Locate and identify every blood parasite.
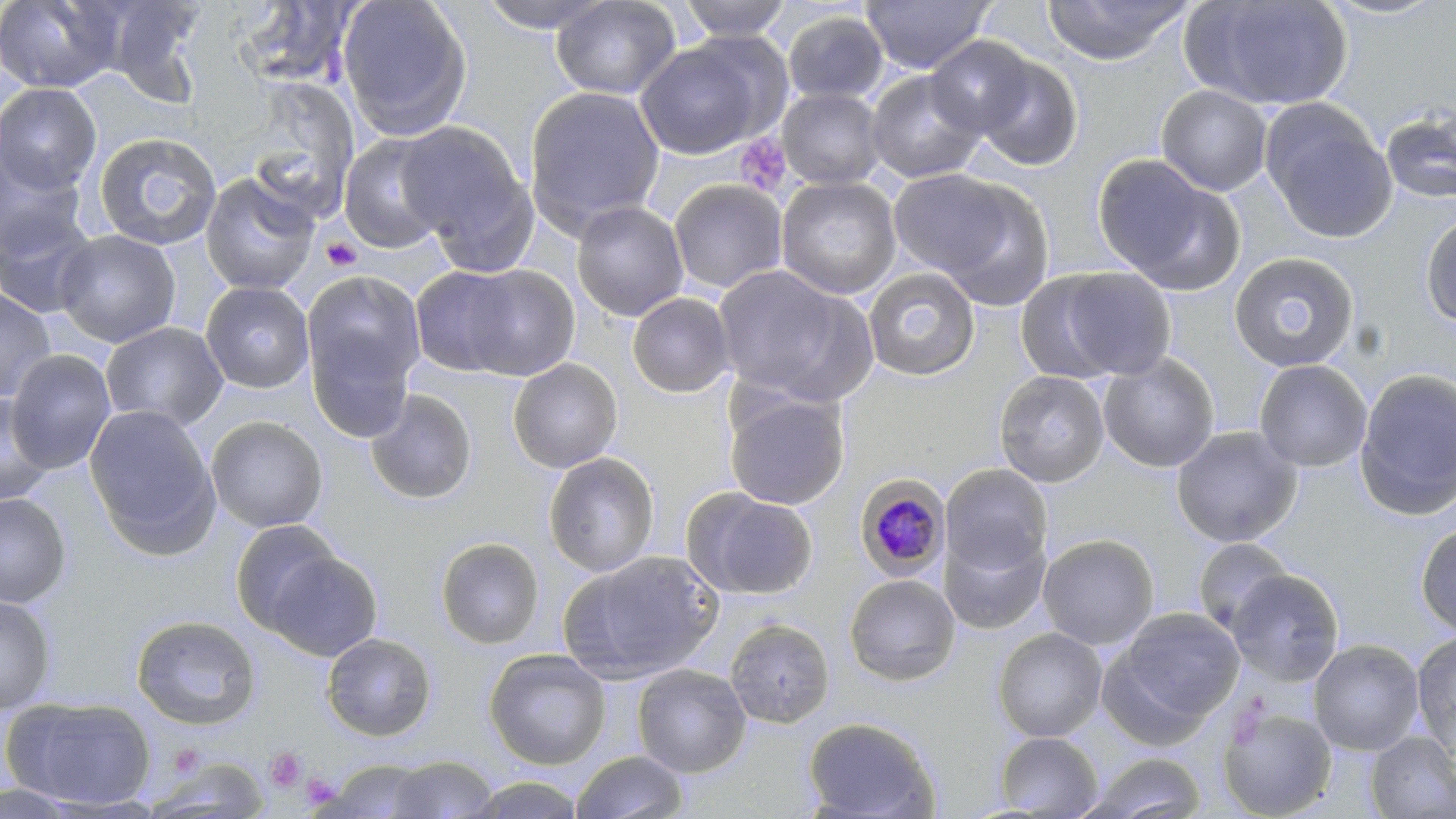

Approximate bounding boxes as [x1, y1, x2, y2] in pixels.
Plasmodium malariae-infected red blood cells: [853, 474, 952, 579].
No Plasmodium falciparum, Plasmodium ovale, Plasmodium vivax, Babesia divergens, or Trypanosoma brucei observed.

Summary:
  - Uninfected red blood cell locations: [0, 0, 123, 94], [96, 0, 208, 105], [336, 0, 473, 140], [475, 0, 619, 33], [550, 0, 681, 100], [677, 0, 793, 41], [860, 0, 994, 74], [1041, 0, 1192, 65], [1185, 0, 1355, 111], [1318, 0, 1451, 20], [234, 1, 359, 90], [782, 10, 889, 105], [924, 35, 1038, 138], [635, 39, 769, 159], [970, 51, 1084, 172], [866, 70, 986, 183], [245, 81, 361, 220], [0, 82, 102, 194], [1156, 85, 1272, 196], [524, 86, 666, 235], [777, 88, 886, 189], [1263, 104, 1398, 243], [1380, 108, 1456, 206], [394, 120, 533, 255], [93, 131, 222, 250], [339, 134, 449, 253], [0, 149, 89, 261], [1092, 154, 1243, 294], [888, 169, 1021, 281], [200, 173, 320, 296], [776, 177, 902, 299], [929, 179, 1055, 311], [668, 180, 788, 294], [571, 201, 689, 321], [0, 210, 98, 318], [1420, 210, 1456, 329], [54, 229, 181, 348], [1229, 252, 1359, 372], [454, 264, 580, 380], [713, 264, 855, 398], [410, 266, 523, 377], [861, 266, 981, 381], [1036, 266, 1179, 382], [301, 268, 426, 419], [200, 281, 314, 394], [0, 288, 56, 402], [627, 292, 735, 398], [101, 321, 228, 432], [4, 349, 117, 474], [1098, 353, 1220, 472], [508, 358, 623, 473], [1253, 359, 1373, 472], [1355, 368, 1456, 520], [994, 370, 1110, 487], [365, 389, 478, 505], [1, 390, 55, 507], [723, 391, 850, 510], [84, 404, 219, 551], [205, 416, 328, 533], [1171, 426, 1303, 547], [543, 452, 660, 576], [941, 463, 1053, 578], [687, 489, 818, 600], [0, 494, 71, 608], [229, 519, 343, 634], [1415, 523, 1456, 638], [940, 527, 1050, 635], [1038, 534, 1159, 650], [436, 537, 544, 649], [1193, 537, 1295, 636], [265, 550, 382, 661], [563, 551, 721, 682], [1227, 569, 1344, 686], [844, 573, 961, 687], [0, 593, 56, 714], [1104, 609, 1243, 737], [131, 615, 261, 730], [724, 618, 835, 728], [993, 627, 1107, 742], [1411, 631, 1456, 756], [321, 633, 437, 741], [1308, 639, 1425, 755], [484, 648, 611, 770], [632, 665, 751, 777], [7, 697, 157, 810], [1218, 706, 1337, 819], [802, 716, 941, 818], [1364, 731, 1456, 818], [996, 732, 1104, 817], [570, 750, 688, 819], [1084, 752, 1206, 818], [387, 756, 498, 817], [147, 757, 271, 817], [324, 759, 435, 818], [467, 774, 586, 818], [0, 784, 84, 819]
  - Platelet locations: [735, 134, 791, 195], [321, 236, 362, 272], [1226, 697, 1271, 748], [264, 746, 308, 793], [300, 772, 341, 808]
  - Slide-level diagnosis: Plasmodium malariae
  - Stain: May-Grünwald-Giemsa
  - Image size: 1456×819 pixels
  - Modality: light microscopy
  - Magnification: 1000x
  - Preparation: thin blood film
  - Field of view: single